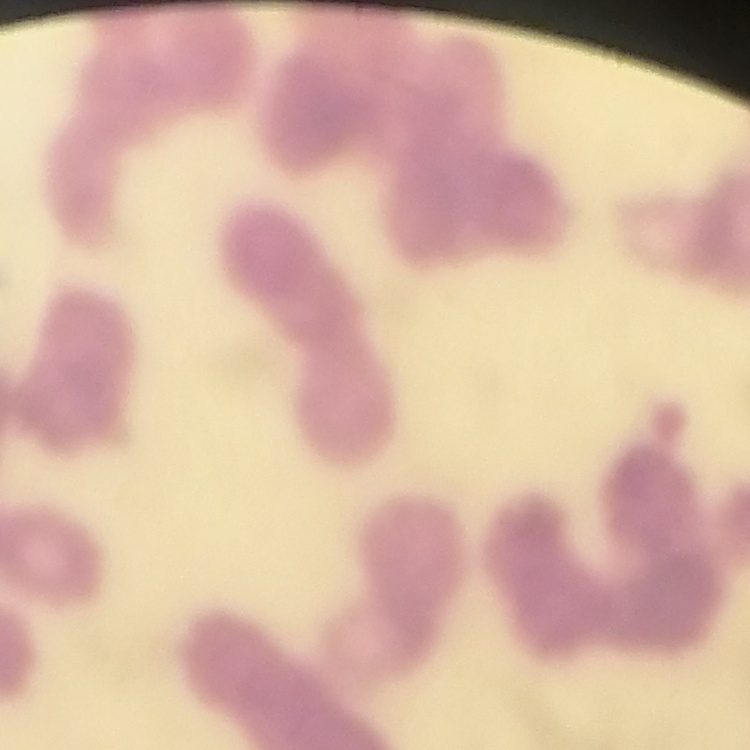

The erythrocytes exhibit rouleaux formation. Field's or Giemsa stain. One tile cut from a larger photomicrograph. Thin blood film.